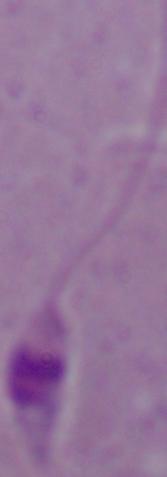

Summary:
  - Magnification: 1000x
  - Identification: Leishmania
  - Modality: micrograph